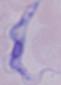
Summary:
  - Identification: trypanosome
  - Magnification: 1000x
  - Modality: micrograph